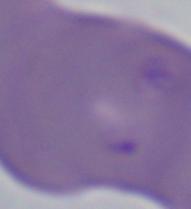
modality: micrograph
magnification: 1000x
identification: Babesia